Outline each white blood cell.
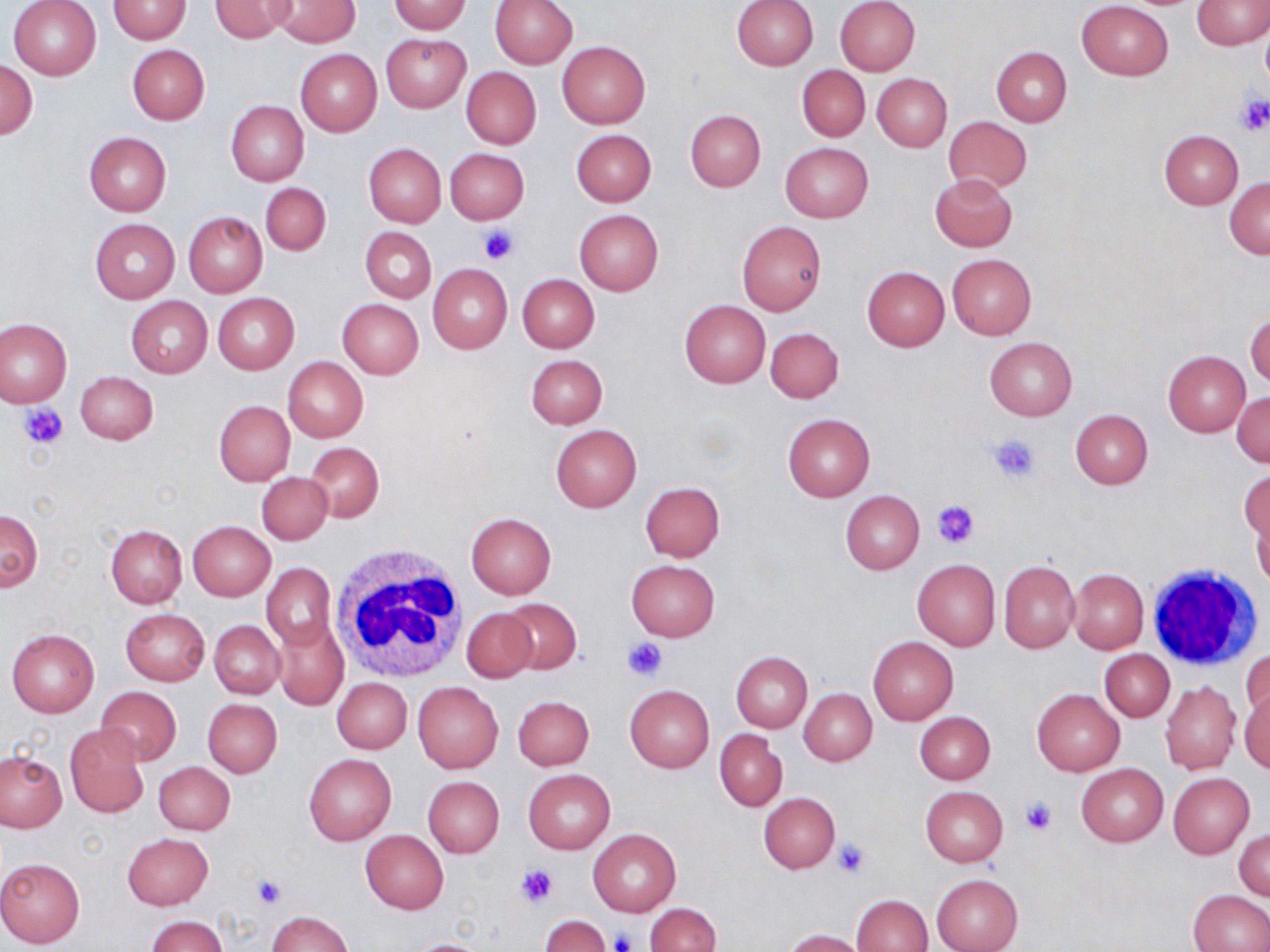
Approximate bounding boxes as (x1, y1, x2, y2) in pixels.
White blood cells: (330, 542, 470, 688), (1144, 563, 1262, 670).

Summary:
  - Uninfected red blood cell locations: (8, 0, 102, 80), (106, 0, 191, 43), (209, 0, 296, 42), (267, 0, 360, 48), (835, 0, 920, 75), (1191, 0, 1269, 49), (386, 1, 472, 34), (489, 1, 578, 67), (730, 1, 818, 71), (1076, 1, 1173, 80), (1259, 26, 1270, 89), (380, 34, 471, 113), (558, 41, 651, 128), (127, 44, 209, 124), (991, 47, 1072, 125), (295, 50, 382, 136), (2, 61, 37, 138), (796, 64, 870, 142), (461, 67, 541, 149), (872, 74, 952, 152), (226, 100, 309, 186), (685, 109, 765, 191), (944, 117, 1032, 194), (570, 129, 656, 206), (1159, 129, 1243, 209), (84, 132, 171, 215), (780, 142, 873, 223), (363, 143, 446, 227), (444, 148, 528, 223), (928, 174, 1017, 252), (1225, 177, 1270, 259), (260, 182, 330, 256), (574, 210, 663, 295), (182, 211, 267, 298), (90, 218, 179, 302), (737, 221, 826, 316), (361, 226, 436, 303), (946, 253, 1036, 339), (429, 265, 513, 353), (861, 266, 950, 351), (518, 274, 600, 352), (213, 292, 299, 374), (125, 296, 212, 378), (338, 299, 423, 379), (679, 300, 770, 388), (1247, 309, 1270, 387), (0, 317, 72, 407), (765, 326, 843, 404), (984, 337, 1077, 420), (1164, 350, 1250, 436), (527, 355, 607, 428), (283, 357, 367, 442), (76, 371, 159, 445), (1233, 393, 1269, 467), (214, 401, 295, 485), (1071, 409, 1153, 489), (783, 413, 875, 500), (550, 425, 642, 512), (307, 442, 383, 521), (1240, 469, 1269, 549), (257, 471, 332, 544), (639, 481, 725, 561), (840, 490, 924, 574), (0, 509, 42, 590), (1253, 511, 1269, 589), (466, 512, 556, 598), (187, 521, 275, 600), (107, 525, 187, 607), (626, 559, 718, 641), (912, 559, 1000, 652), (999, 560, 1079, 652), (261, 562, 335, 650), (1068, 569, 1148, 653), (499, 598, 582, 674), (120, 608, 210, 686), (461, 608, 539, 683), (272, 618, 348, 710), (210, 620, 285, 699), (6, 627, 99, 718), (868, 636, 958, 725), (1101, 650, 1174, 721), (1241, 650, 1270, 724), (730, 651, 813, 732), (332, 677, 412, 754), (412, 682, 503, 773), (1160, 682, 1240, 774), (624, 685, 714, 772), (96, 686, 181, 765), (1240, 686, 1269, 772), (799, 688, 876, 766), (1032, 688, 1125, 776), (518, 692, 601, 853), (513, 695, 593, 770), (203, 697, 282, 777), (915, 711, 995, 785), (64, 724, 149, 818), (714, 730, 787, 810), (0, 752, 66, 831), (304, 754, 396, 845), (154, 761, 235, 835), (1076, 763, 1168, 847), (523, 770, 614, 853), (1168, 773, 1254, 858), (424, 776, 504, 857), (920, 786, 1008, 866), (758, 792, 839, 873), (588, 828, 680, 916), (1235, 828, 1269, 900), (360, 830, 449, 914), (122, 833, 214, 910), (0, 857, 86, 949), (931, 873, 1023, 952), (1187, 890, 1270, 952), (851, 894, 932, 951), (645, 902, 720, 952), (265, 912, 355, 952), (539, 915, 609, 952), (147, 916, 227, 952), (785, 929, 869, 952), (405, 938, 490, 951)
  - Platelet locations: (1235, 93, 1270, 136), (478, 224, 519, 264), (19, 401, 69, 448), (987, 432, 1042, 482), (931, 501, 978, 548), (621, 636, 668, 682), (1020, 797, 1058, 835), (832, 838, 871, 876), (516, 864, 558, 907), (248, 872, 288, 910), (607, 930, 636, 952)
  - Slide-level diagnosis: negative for blood parasites
  - Image size: 1270×952 pixels
  - Field of view: one of a larger specimen
  - Stain: May-Grünwald-Giemsa
  - Magnification: 1000x
  - Preparation: thin blood smear
  - Modality: light microscopy